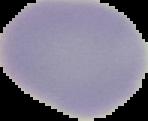

Summary:
  - Preparation: thin blood film
  - Result: no Plasmodium parasites seen
  - Image type: segmented cell region with the area outside set to black
  - Image size: 148×121 pixels